Identify the cell.
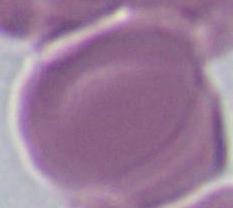

This is an erythrocyte.

Summary:
  - Magnification: 1000x
  - Modality: micrograph